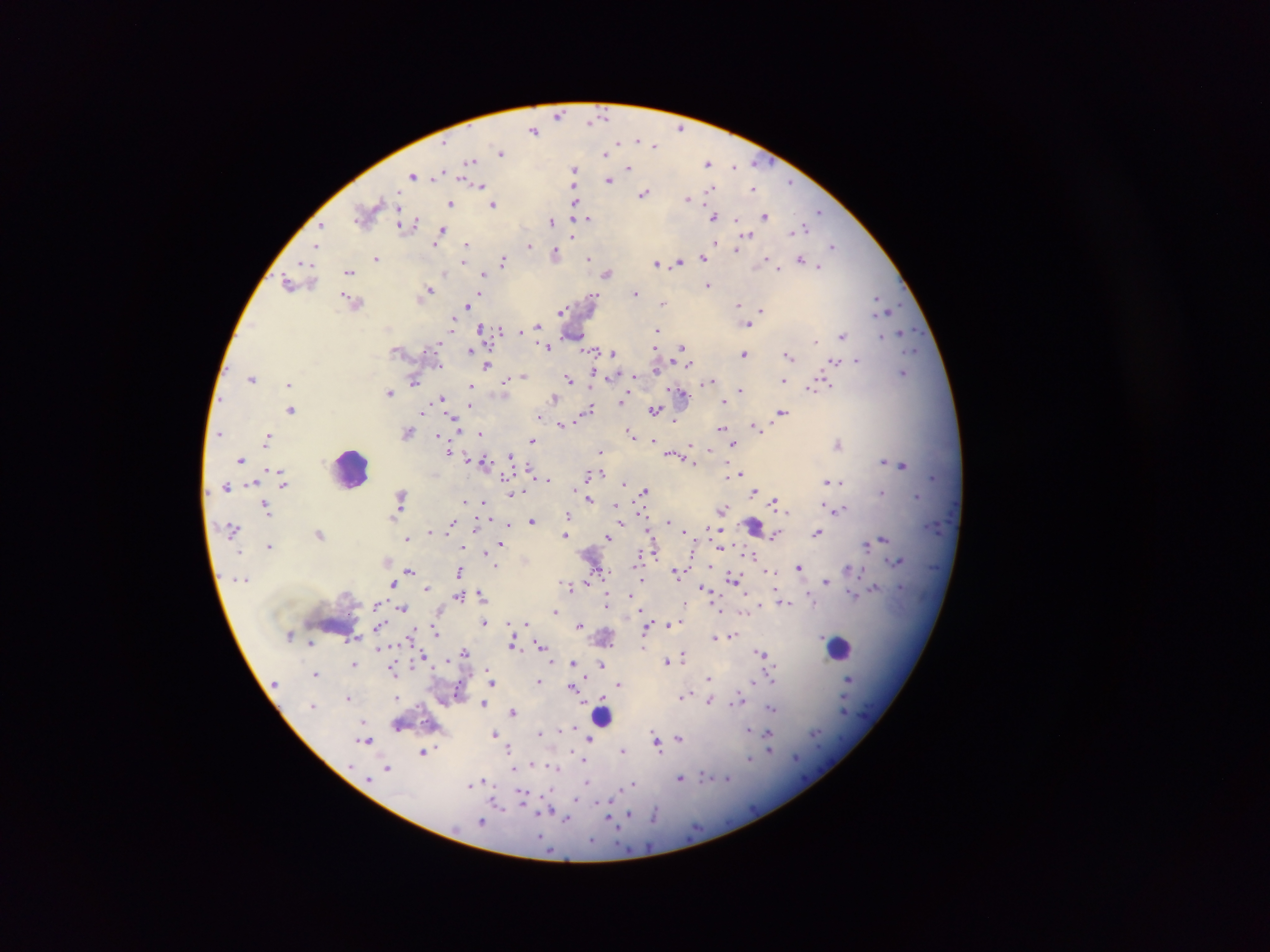

Approximate centers as {x, y} in pixels. Leukocyte locations: {346, 470}, {334, 624}, {838, 650}. Plasmodium parasite locations: {604, 112}, {560, 114}, {592, 122}, {681, 127}, {531, 132}, {638, 139}, {619, 141}, {656, 144}, {501, 153}, {608, 153}, {471, 162}, {755, 163}, {707, 164}, {734, 167}, {629, 168}, {576, 170}, {437, 172}, {414, 177}, {462, 177}, {608, 179}, {466, 181}, {788, 182}, {481, 184}, {576, 186}, {753, 187}, {709, 188}, {644, 196}, {688, 199}, {575, 201}, {449, 204}, {495, 204}, {398, 208}, {821, 211}, {767, 214}, {713, 216}, {588, 218}, {734, 220}, {401, 221}, {415, 221}, {551, 221}, {321, 224}, {805, 228}, {442, 229}, {748, 237}, {466, 244}, {530, 245}, {832, 245}, {315, 246}, {735, 249}, {555, 251}, {701, 257}, {375, 258}, {591, 258}, {767, 258}, {798, 259}, {502, 261}, {463, 262}, {677, 262}, {304, 264}, {656, 264}, {821, 266}, {778, 267}, {445, 272}, {350, 273}, {483, 274}, {608, 275}, {708, 284}, {289, 286}, {431, 289}, {478, 294}, {638, 294}, {600, 295}, {346, 297}, {878, 297}, {662, 304}, {467, 305}, {737, 306}, {892, 309}, {561, 310}, {761, 310}, {452, 324}, {750, 324}, {536, 325}, {479, 327}, {657, 328}, {501, 330}, {518, 330}, {900, 330}, {843, 336}, {881, 337}, {815, 341}, {441, 344}, {682, 345}, {547, 347}, {470, 348}, {588, 349}, {593, 350}, {915, 350}, {424, 351}, {612, 353}, {743, 353}, {790, 355}, {615, 356}, {856, 360}, {688, 363}, {834, 364}, {487, 366}, {656, 367}, {443, 368}, {905, 372}, {522, 376}, {251, 377}, {819, 377}, {609, 378}, {567, 379}, {506, 381}, {708, 381}, {781, 381}, {415, 382}, {289, 385}, {470, 385}, {828, 386}, {741, 391}, {808, 391}, {391, 392}, {683, 395}, {552, 397}, {441, 398}, {622, 398}, {724, 399}, {621, 402}, {467, 405}, {590, 408}, {290, 410}, {654, 410}, {782, 411}, {424, 413}, {540, 417}, {452, 420}, {561, 424}, {755, 426}, {720, 429}, {218, 433}, {479, 433}, {440, 434}, {631, 435}, {268, 437}, {533, 439}, {653, 441}, {732, 442}, {839, 445}, {690, 446}, {448, 449}, {599, 452}, {672, 453}, {510, 456}, {470, 459}, {692, 460}, {883, 461}, {240, 462}, {482, 462}, {902, 465}, {528, 470}, {741, 471}, {283, 474}, {590, 474}, {505, 476}, {726, 476}, {934, 478}, {548, 479}, {840, 480}, {932, 480}, {828, 481}, {830, 483}, {626, 485}, {246, 486}, {285, 486}, {226, 487}, {645, 489}, {755, 491}, {401, 492}, {882, 494}, {512, 495}, {916, 495}, {590, 499}, {483, 501}, {775, 501}, {465, 502}, {617, 504}, {266, 505}, {823, 505}, {723, 510}, {839, 510}, {567, 514}, {398, 515}, {531, 520}, {622, 520}, {451, 521}, {670, 521}, {229, 525}, {476, 525}, {754, 526}, {510, 527}, {931, 527}, {648, 530}, {714, 531}, {687, 532}, {818, 532}, {649, 534}, {564, 535}, {605, 536}, {774, 536}, {883, 537}, {408, 539}, {502, 542}, {867, 544}, {269, 545}, {464, 546}, {719, 549}, {239, 552}, {488, 553}, {654, 554}, {753, 556}, {636, 560}, {897, 561}, {497, 566}, {799, 566}, {847, 569}, {409, 570}, {863, 570}, {593, 571}, {766, 571}, {458, 572}, {676, 573}, {730, 578}, {233, 580}, {827, 582}, {391, 584}, {567, 585}, {876, 585}, {427, 587}, {704, 588}, {480, 591}, {630, 594}, {854, 596}, {459, 597}, {605, 599}, {606, 603}, {786, 603}, {686, 605}, {402, 606}, {376, 608}, {555, 612}, {527, 621}, {485, 622}, {579, 624}, {670, 624}, {646, 627}, {372, 630}, {434, 633}, {734, 633}, {646, 635}, {411, 636}, {716, 638}, {309, 644}, {513, 644}, {540, 645}, {643, 647}, {762, 650}, {464, 651}, {684, 655}, {425, 657}, {667, 661}, {575, 662}, {353, 664}, {602, 664}, {392, 672}, {316, 673}, {773, 676}, {708, 677}, {849, 677}, {494, 681}, {539, 681}, {754, 682}, {620, 684}, {570, 685}, {455, 693}, {685, 696}, {347, 697}, {581, 700}, {737, 701}, {484, 702}, {710, 702}, {313, 704}, {846, 707}, {773, 709}, {511, 710}, {602, 717}, {561, 728}, {571, 728}, {749, 729}, {541, 731}, {497, 732}, {654, 733}, {815, 734}, {655, 738}, {678, 738}, {368, 740}, {591, 740}, {657, 747}, {623, 749}, {510, 750}, {421, 752}, {770, 752}, {750, 757}, {796, 758}, {534, 765}, {387, 767}, {351, 768}, {511, 768}, {555, 770}, {681, 778}, {705, 778}, {727, 779}, {368, 780}, {484, 780}, {586, 781}, {632, 783}, {472, 784}, {520, 792}, {522, 798}, {575, 800}, {495, 803}, {601, 803}, {500, 806}, {534, 811}, {548, 813}, {629, 813}, {609, 818}, {567, 819}, {482, 821}, {614, 824}, {618, 833}, {540, 837}. Image is 1270×952 pixels. Sample from Ghana. Thick blood smear. Mobile-phone photograph taken through the microscope. One field of view.